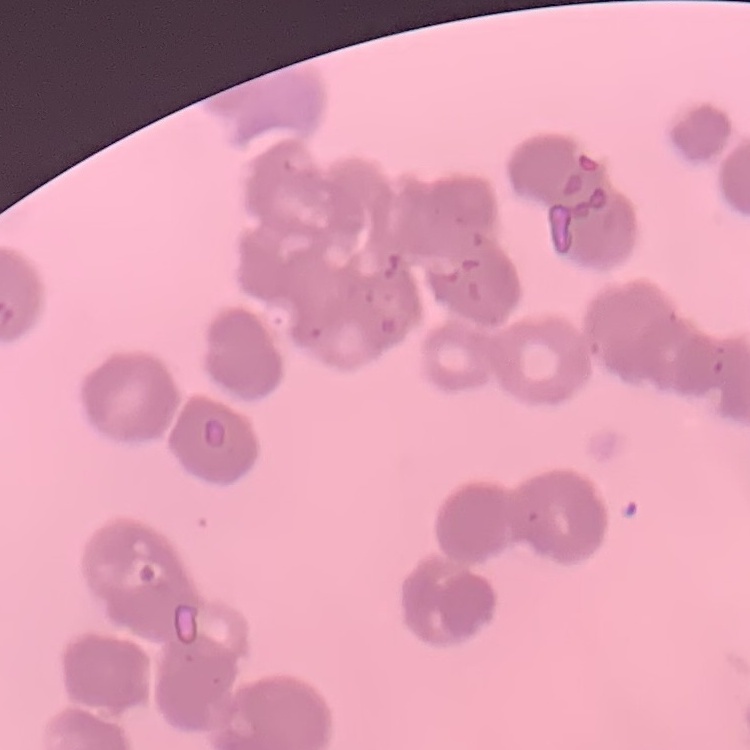
The red blood cells show rouleaux formation. Thin peripheral smear. Field's or Giemsa stain. One tile cut from a larger photomicrograph.